Locate and identify every blood parasite.
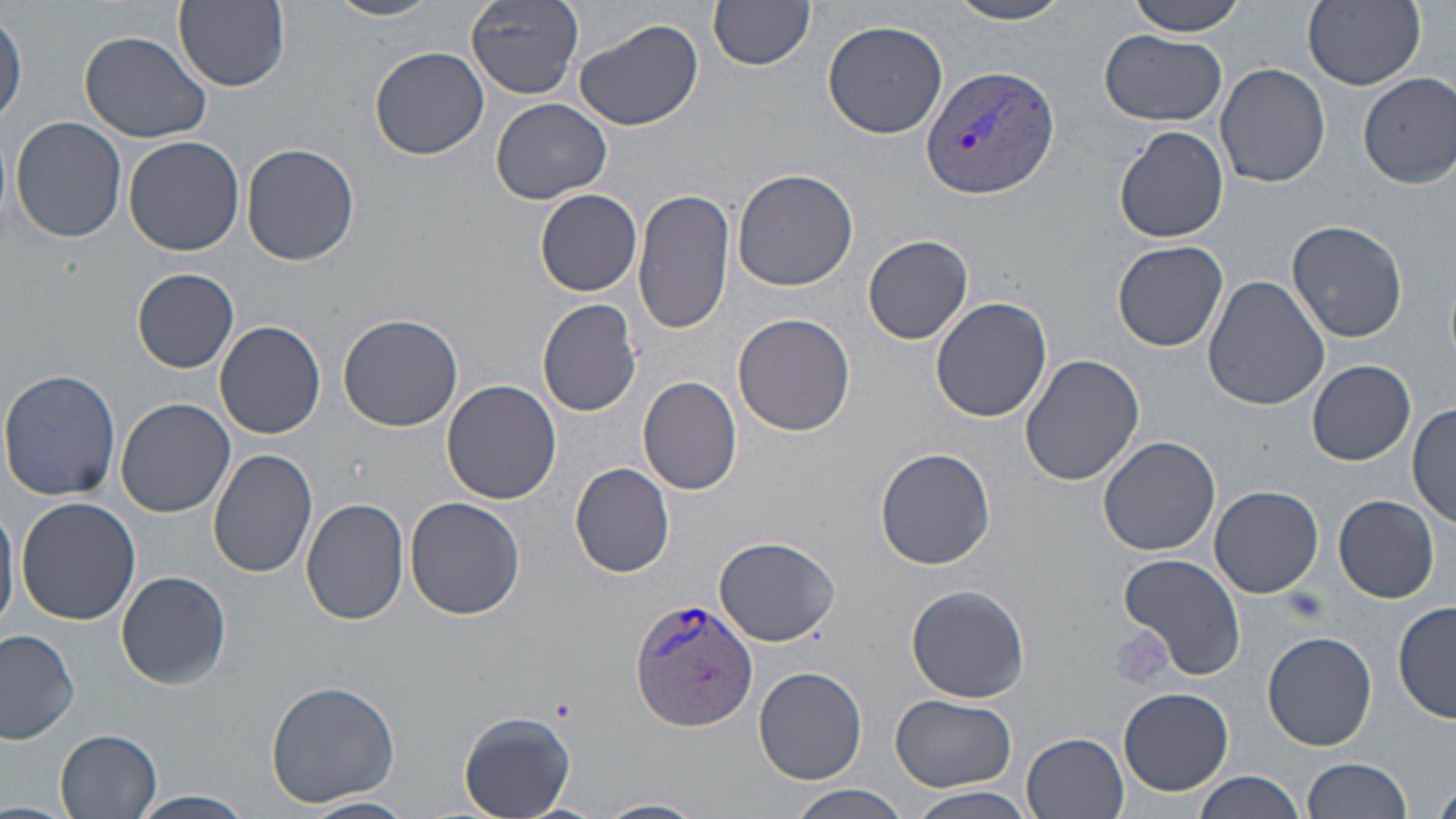
Approximate bounding boxes as [x1, y1, x2, y2] in pixels.
Plasmodium vivax-infected red blood cells: [920, 65, 1061, 199], [629, 597, 758, 732].
No Plasmodium falciparum, Plasmodium ovale, Plasmodium malariae, Babesia divergens, or Trypanosoma brucei observed.

slide-level diagnosis = Plasmodium vivax
uninfected red blood cell locations = approximate bounding boxes as [x1, y1, x2, y2] in pixels: [174, 0, 290, 90], [327, 0, 445, 21], [466, 0, 584, 99], [1126, 0, 1247, 36], [1304, 0, 1426, 90], [945, 1, 1079, 25], [709, 2, 815, 71], [1, 10, 25, 125], [574, 17, 704, 132], [821, 19, 949, 138], [1100, 30, 1229, 125], [79, 31, 212, 143], [370, 46, 489, 160], [1214, 62, 1330, 188], [1357, 73, 1455, 187], [491, 98, 612, 204], [9, 115, 128, 243], [1115, 125, 1230, 243], [123, 135, 246, 256], [242, 142, 360, 266], [732, 167, 858, 291], [535, 189, 643, 296], [633, 189, 736, 336], [1285, 219, 1410, 344], [862, 234, 973, 345], [1112, 240, 1229, 351], [132, 268, 239, 373], [1201, 276, 1329, 411], [930, 297, 1054, 424], [536, 299, 642, 418], [336, 313, 464, 431], [733, 313, 856, 436], [213, 319, 326, 439], [1020, 354, 1144, 485], [1307, 359, 1415, 465], [0, 368, 122, 502], [637, 375, 743, 495], [442, 378, 562, 503], [116, 397, 234, 517], [1407, 404, 1456, 528], [1097, 434, 1221, 556], [875, 446, 997, 570], [208, 448, 319, 578], [570, 462, 676, 578], [1209, 485, 1323, 598], [1333, 496, 1439, 603], [0, 497, 19, 637], [16, 497, 141, 625], [301, 497, 410, 626], [406, 498, 525, 621], [713, 536, 841, 645], [1118, 552, 1246, 681], [116, 571, 231, 689], [907, 584, 1030, 704], [1394, 601, 1455, 723], [0, 628, 81, 744], [1262, 632, 1377, 750], [753, 666, 868, 784], [265, 679, 401, 808], [1117, 687, 1234, 797], [891, 695, 1018, 792], [457, 710, 575, 817], [55, 730, 162, 819], [1023, 732, 1130, 817], [1303, 757, 1413, 819], [1193, 773, 1306, 819], [1434, 780, 1456, 819], [788, 785, 913, 818], [903, 787, 1039, 818], [130, 790, 258, 819], [298, 795, 415, 818], [592, 797, 707, 819], [0, 800, 75, 819]
magnification = 1000x
modality = light microscopy
field of view = single
stain = May-Grünwald-Giemsa
image size = 1456×819 pixels
platelet locations = approximate bounding boxes as [x1, y1, x2, y2] in pixels: [1283, 584, 1329, 623], [1110, 626, 1173, 691]
preparation = thin blood film